Assess this cell for malaria.
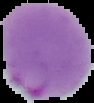
It is parasitized.

{
  "image_size": "94×103 pixels",
  "preparation": "thin blood smear",
  "image_type": "segmented cell region with the area outside set to black"
}